State the preparation type.
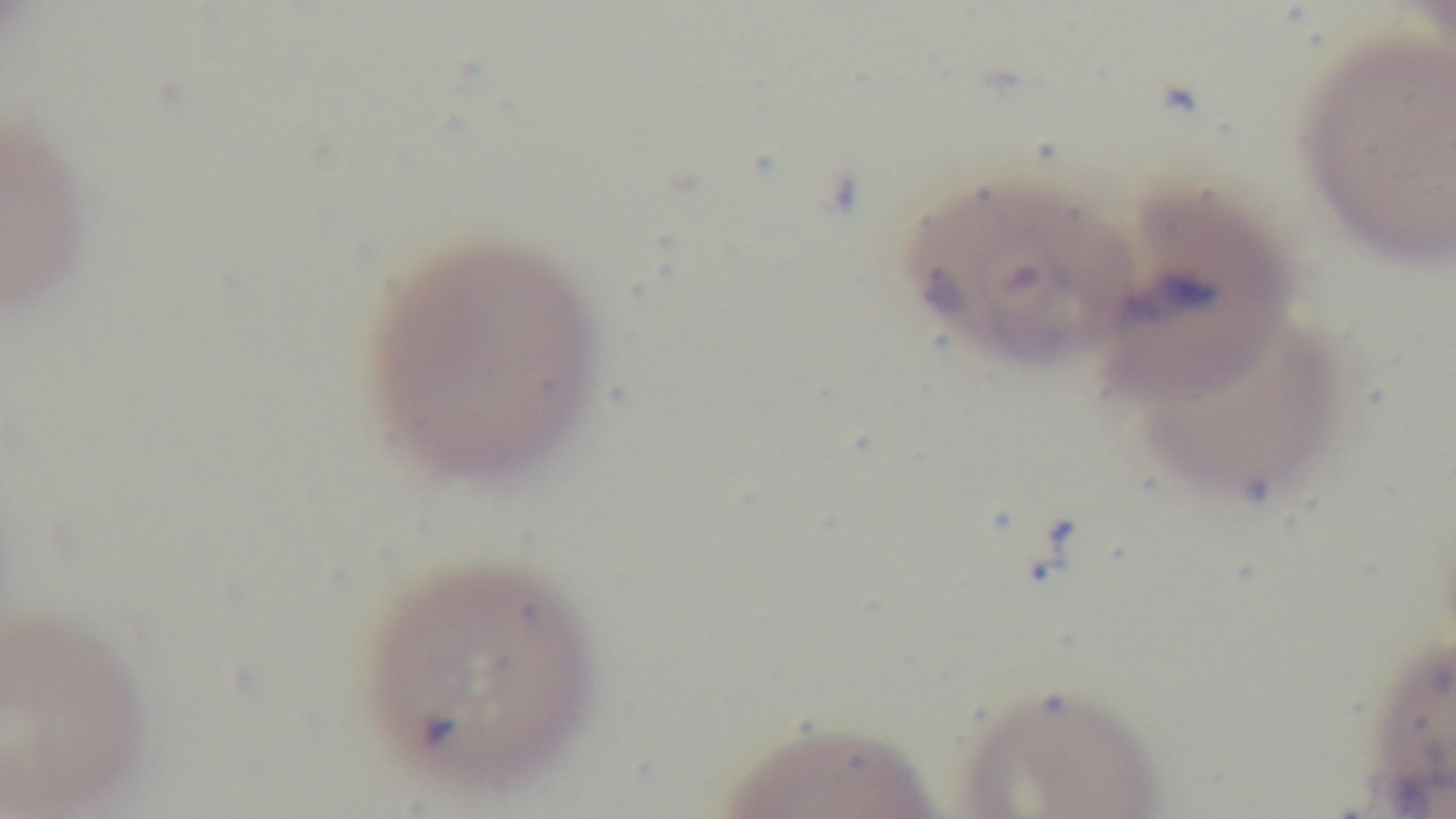

A thin smear.

One field from the slide. Photomicrograph. Malaria status: infected. Captured with a mounted 4K digital camera. 100x oil-immersion objective. Giemsa stain.